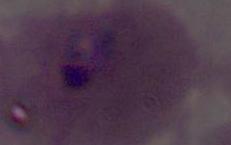
Summary:
  - Modality: photomicrograph
  - Identification: Plasmodium
  - Magnification: 400x or 1000x